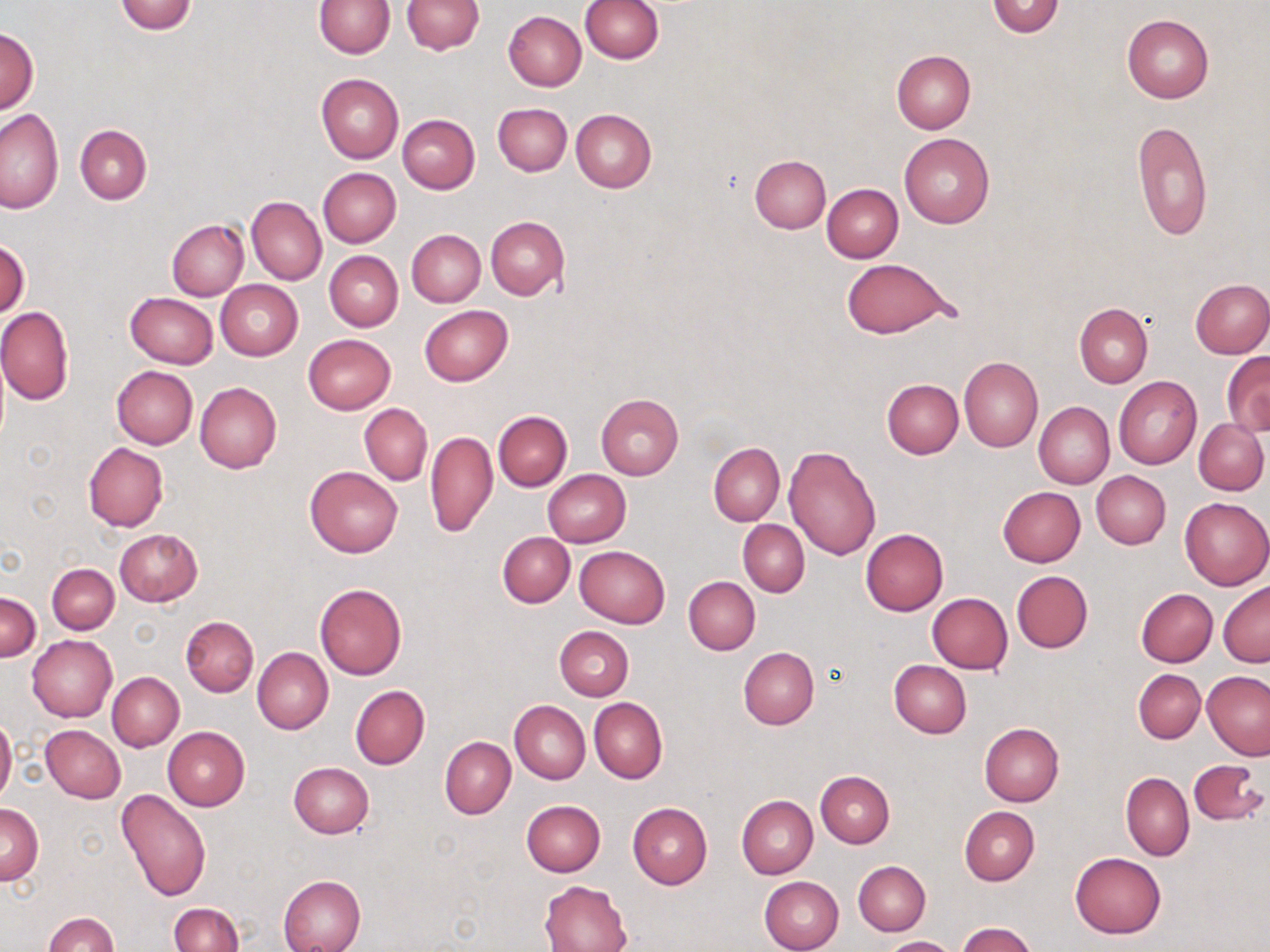
Summary:
  - Coordinate format: approximate bounding boxes as named x1/y1/x2/y2 corners in pixels
  - Uninfected red blood cell locations: (x1=114, y1=0, x2=198, y2=35), (x1=316, y1=0, x2=393, y2=57), (x1=401, y1=0, x2=482, y2=55), (x1=579, y1=0, x2=662, y2=63), (x1=987, y1=0, x2=1065, y2=38), (x1=501, y1=7, x2=661, y2=78), (x1=503, y1=11, x2=585, y2=91), (x1=1122, y1=14, x2=1215, y2=103), (x1=1, y1=26, x2=38, y2=113), (x1=891, y1=50, x2=975, y2=134), (x1=316, y1=73, x2=403, y2=162), (x1=493, y1=102, x2=572, y2=176), (x1=0, y1=106, x2=63, y2=214), (x1=571, y1=109, x2=656, y2=192), (x1=398, y1=114, x2=480, y2=193), (x1=1132, y1=120, x2=1213, y2=242), (x1=75, y1=124, x2=152, y2=203), (x1=899, y1=133, x2=995, y2=227), (x1=750, y1=155, x2=830, y2=233), (x1=318, y1=168, x2=401, y2=248), (x1=822, y1=184, x2=903, y2=262), (x1=247, y1=196, x2=326, y2=285), (x1=486, y1=216, x2=569, y2=301), (x1=167, y1=220, x2=249, y2=300), (x1=407, y1=229, x2=486, y2=307), (x1=0, y1=238, x2=30, y2=319), (x1=324, y1=251, x2=402, y2=331), (x1=842, y1=258, x2=952, y2=338), (x1=1190, y1=279, x2=1270, y2=357), (x1=215, y1=280, x2=302, y2=361), (x1=125, y1=292, x2=218, y2=369), (x1=1074, y1=303, x2=1153, y2=387), (x1=419, y1=305, x2=512, y2=386), (x1=0, y1=307, x2=74, y2=405), (x1=302, y1=334, x2=396, y2=414), (x1=1222, y1=353, x2=1270, y2=436), (x1=960, y1=357, x2=1043, y2=452), (x1=111, y1=366, x2=198, y2=449), (x1=1114, y1=376, x2=1203, y2=470), (x1=882, y1=378, x2=964, y2=458), (x1=195, y1=382, x2=282, y2=473), (x1=596, y1=394, x2=684, y2=479), (x1=1033, y1=402, x2=1114, y2=490), (x1=359, y1=404, x2=432, y2=484), (x1=493, y1=410, x2=573, y2=491), (x1=1195, y1=418, x2=1269, y2=494), (x1=426, y1=430, x2=498, y2=538), (x1=83, y1=443, x2=168, y2=532), (x1=709, y1=443, x2=784, y2=525), (x1=784, y1=445, x2=882, y2=560), (x1=304, y1=465, x2=403, y2=558), (x1=543, y1=469, x2=631, y2=546), (x1=1091, y1=471, x2=1171, y2=549), (x1=997, y1=486, x2=1086, y2=566), (x1=1180, y1=497, x2=1270, y2=590), (x1=738, y1=520, x2=809, y2=596), (x1=861, y1=528, x2=949, y2=615), (x1=114, y1=529, x2=203, y2=606), (x1=497, y1=532, x2=574, y2=607), (x1=575, y1=546, x2=670, y2=628), (x1=47, y1=563, x2=119, y2=634), (x1=1011, y1=570, x2=1092, y2=652), (x1=684, y1=576, x2=760, y2=655), (x1=1219, y1=581, x2=1270, y2=667), (x1=315, y1=583, x2=407, y2=680), (x1=1136, y1=588, x2=1218, y2=667), (x1=0, y1=593, x2=41, y2=660), (x1=928, y1=593, x2=1013, y2=673), (x1=181, y1=616, x2=258, y2=697), (x1=554, y1=626, x2=634, y2=700), (x1=27, y1=635, x2=117, y2=722), (x1=252, y1=647, x2=333, y2=734), (x1=738, y1=648, x2=819, y2=729), (x1=889, y1=660, x2=971, y2=738), (x1=1133, y1=669, x2=1205, y2=743), (x1=1202, y1=670, x2=1270, y2=760), (x1=107, y1=671, x2=185, y2=752), (x1=351, y1=686, x2=429, y2=769), (x1=589, y1=697, x2=668, y2=784), (x1=509, y1=700, x2=590, y2=784), (x1=0, y1=714, x2=17, y2=807), (x1=979, y1=723, x2=1063, y2=807), (x1=41, y1=724, x2=126, y2=802), (x1=162, y1=726, x2=250, y2=811), (x1=440, y1=736, x2=515, y2=818), (x1=1187, y1=759, x2=1268, y2=824), (x1=288, y1=762, x2=374, y2=839), (x1=815, y1=770, x2=894, y2=848), (x1=1121, y1=773, x2=1193, y2=860), (x1=117, y1=789, x2=212, y2=902), (x1=737, y1=795, x2=818, y2=879), (x1=521, y1=800, x2=606, y2=876), (x1=627, y1=803, x2=711, y2=889), (x1=0, y1=805, x2=44, y2=884), (x1=958, y1=807, x2=1038, y2=886), (x1=1069, y1=851, x2=1167, y2=939), (x1=853, y1=860, x2=931, y2=935), (x1=278, y1=875, x2=366, y2=952), (x1=759, y1=875, x2=844, y2=952), (x1=540, y1=880, x2=632, y2=952), (x1=169, y1=903, x2=242, y2=952), (x1=44, y1=912, x2=120, y2=951), (x1=957, y1=923, x2=1038, y2=952), (x1=878, y1=936, x2=959, y2=952)
  - Slide-level diagnosis: no evidence of blood parasites
  - Modality: optical microscopy
  - Image size: 1270×952 pixels
  - Magnification: 1000x
  - Stain: May-Grünwald-Giemsa
  - Preparation: thin blood film
  - Field of view: one of a larger specimen